Assess this cell for malaria.
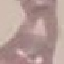
Uninfected.

Giemsa-stained preparation. Photographed with a smartphone camera at the microscope eyepiece. Thin smear of blood. Automatically extracted cell patch, resized to 64 × 64 pixels.